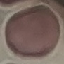 Malaria status: uninfected. Acquired by smartphone through the microscope eyepiece. Thin blood film. Cell patch, automatically extracted from a larger field of view and resized to 64 × 64 pixels. Giemsa-stained preparation.